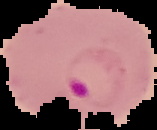
Summary:
  - Image size: 157×130 pixels
  - Preparation: thin blood smear
  - Image type: cell region segmented out of the field of view; surrounding area masked to black
  - Result: Plasmodium parasites detected